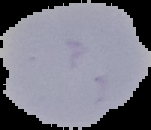

Summary:
  - Preparation: thin blood smear
  - Malaria status: uninfected
  - Image type: segmented cell region on a black background
  - Image size: 151×130 pixels